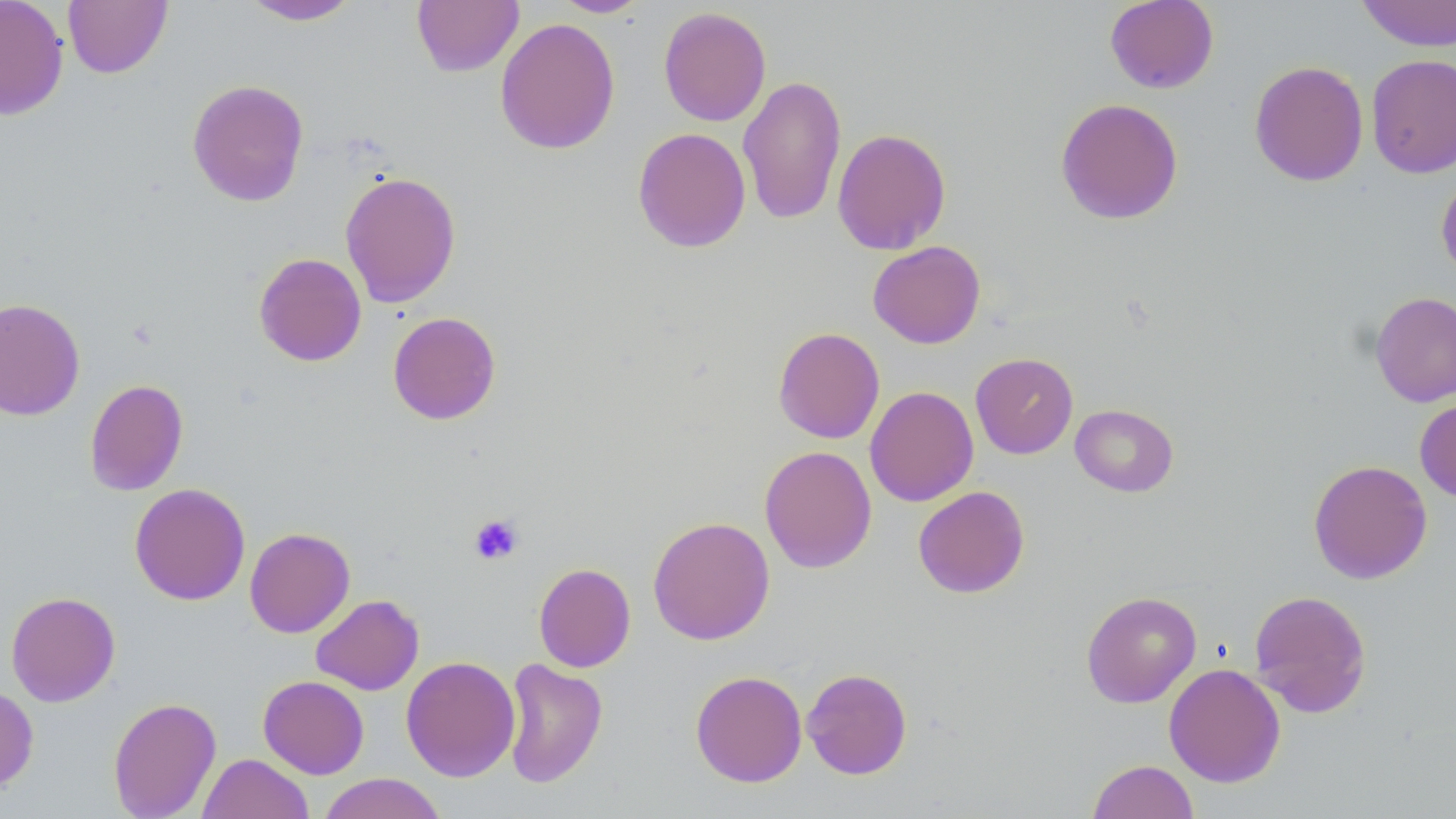
Approximate bounding boxes as (x1,y1)-(x2,y2) corner pairs in pixels. Uninfected red blood cell locations: (0,0)-(69,121), (63,0)-(172,78), (241,0)-(361,25), (412,0)-(524,77), (551,0)-(649,17), (1105,0)-(1219,94), (1356,0)-(1456,52), (658,6)-(771,127), (495,17)-(620,155), (1366,54)-(1456,178), (1249,60)-(1368,187), (738,75)-(847,226), (187,79)-(309,207), (1055,97)-(1184,225), (632,127)-(751,252), (832,127)-(951,254), (340,171)-(461,308), (1436,173)-(1456,280), (868,240)-(986,349), (253,252)-(367,366), (1370,291)-(1456,407), (0,297)-(85,421), (388,311)-(501,425), (773,327)-(885,444), (970,353)-(1078,458), (84,379)-(188,496), (865,386)-(978,507), (1415,398)-(1456,502), (1070,404)-(1179,497), (759,445)-(877,573), (1308,459)-(1433,583), (129,483)-(250,606), (913,486)-(1030,598), (648,516)-(775,645), (244,527)-(355,638), (533,563)-(636,672), (1249,589)-(1372,718), (6,591)-(120,706), (1081,591)-(1202,707), (311,594)-(424,695), (400,655)-(521,781), (501,658)-(608,789), (1163,662)-(1286,788), (801,667)-(913,779), (690,670)-(808,787), (258,675)-(369,779), (0,684)-(39,793), (108,696)-(222,819), (197,753)-(314,819), (1087,759)-(1198,819), (317,772)-(447,819). Platelet locations: (469,513)-(523,565). Slide-level diagnosis: negative for blood parasites. Optical microscopy. May-Grünwald-Giemsa stain. Image is 1456×819 pixels. One field of a larger specimen. Thin blood smear. 1000x magnification.